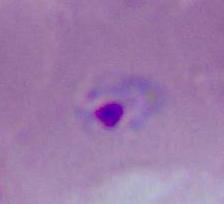

Photomicrograph. A Plasmodium parasite is seen. Captured at either 400x or 1000x magnification.